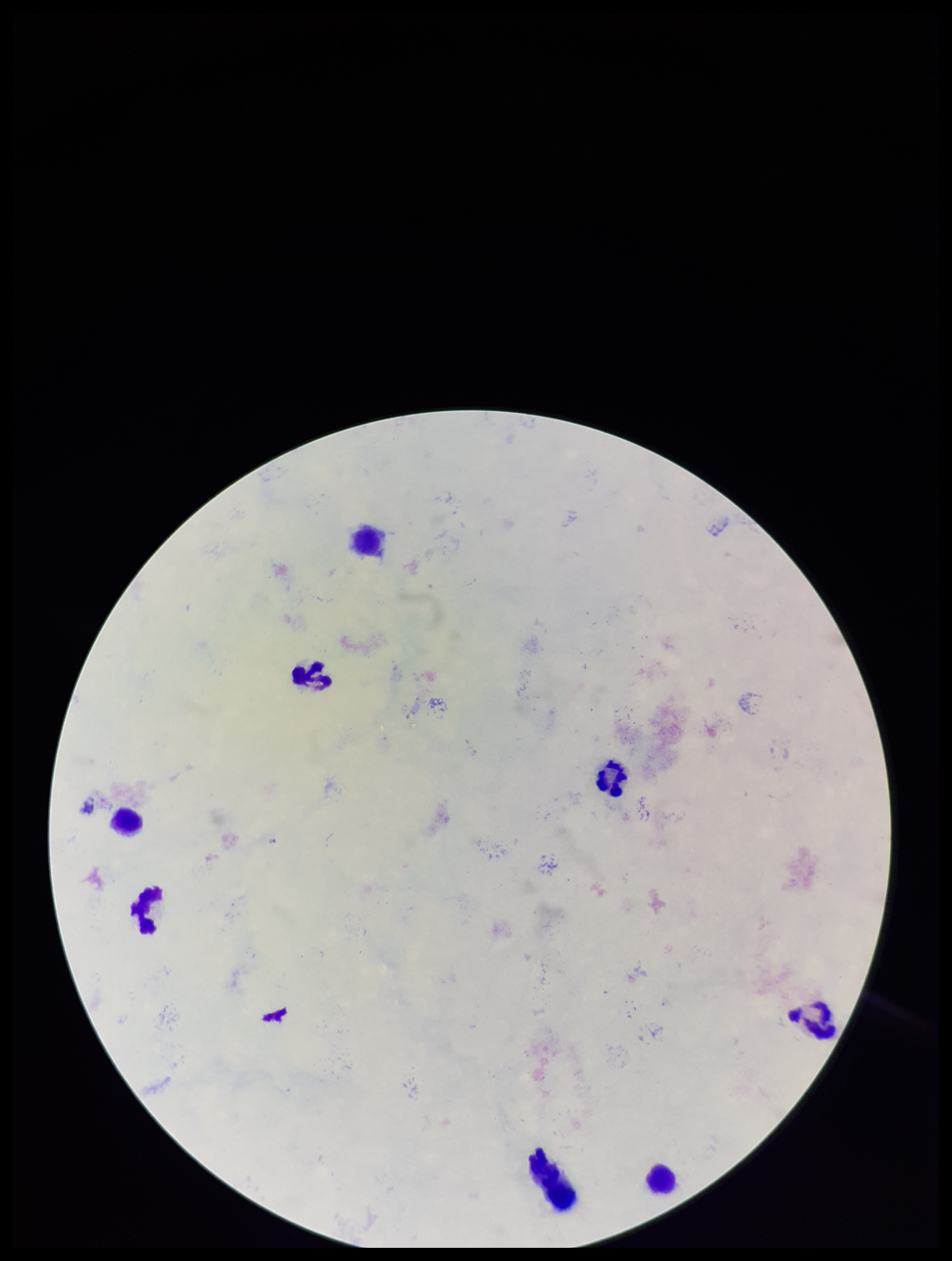
Preparation: thick blood smear. Stained with Giemsa. Image is 952×1261 pixels. One field from this slide. Patient malaria status: negative. Parasite count: 0. Leukocyte count: 7. Smartphone photograph taken through the eyepiece of a microscope. Plasmodium parasites: none detected.